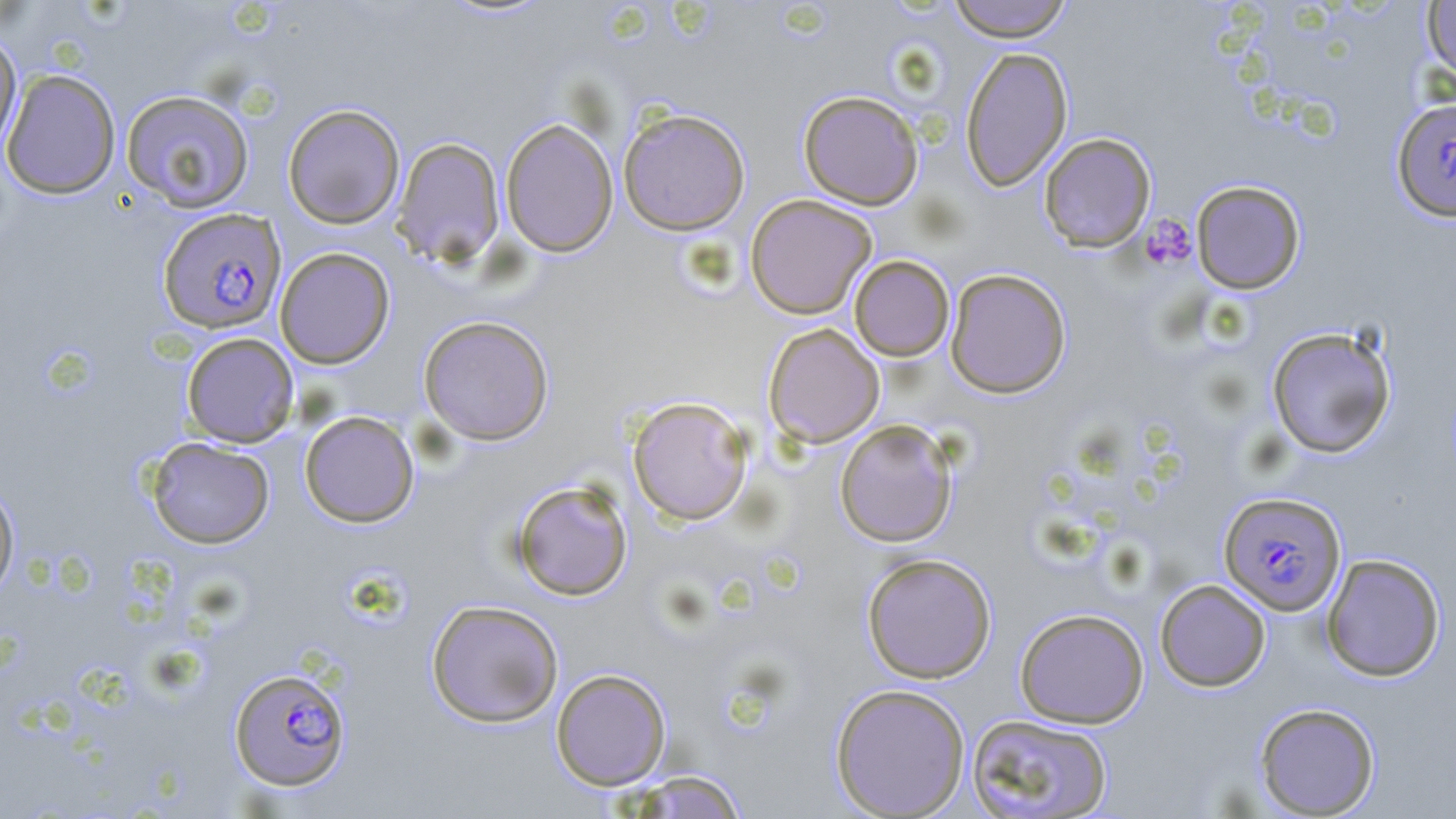

Approximate bounding boxes as [x1, y1, x2, y2] in pixels. Platelet locations: [1140, 214, 1196, 270]. Uninfected red blood cell locations: [946, 0, 1074, 42], [1422, 1, 1455, 82], [0, 31, 23, 155], [960, 46, 1073, 192], [1, 69, 121, 199], [121, 89, 255, 213], [798, 89, 924, 210], [282, 103, 405, 229], [618, 107, 751, 235], [500, 118, 618, 257], [1039, 132, 1156, 252], [392, 137, 505, 266], [1190, 180, 1306, 294], [744, 194, 877, 319], [274, 247, 395, 368], [849, 255, 955, 361], [945, 268, 1071, 398], [418, 315, 555, 445], [763, 323, 885, 448], [1266, 325, 1397, 459], [181, 332, 299, 448], [627, 396, 754, 525], [299, 410, 419, 528], [834, 419, 958, 548], [146, 437, 275, 548], [0, 479, 20, 601], [511, 479, 633, 601], [861, 552, 997, 683], [1321, 553, 1446, 681], [1155, 579, 1271, 691], [426, 599, 564, 728], [1015, 607, 1149, 728], [551, 668, 671, 790], [830, 683, 970, 818], [1254, 702, 1381, 817], [966, 713, 1113, 818], [625, 770, 749, 818]. Plasmodium falciparum-infected red blood cell locations: [1392, 98, 1456, 222], [158, 207, 286, 334], [1219, 491, 1347, 616], [229, 666, 351, 792]. Slide-level diagnosis: Plasmodium falciparum. Captured at 1000x magnification. Single field of view. Image is 1456×819 pixels. May-Grünwald-Giemsa stain. Thin blood smear. Light microscopy.